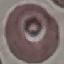
{
  "malaria_status": "uninfected",
  "preparation": "thin blood smear",
  "stain": "Giemsa",
  "image_type": "cell patch, automatically extracted from a larger field of view and resized to 64 × 64 pixels",
  "capture": "smartphone camera at the microscope eyepiece"
}